Name the blood parasite species.
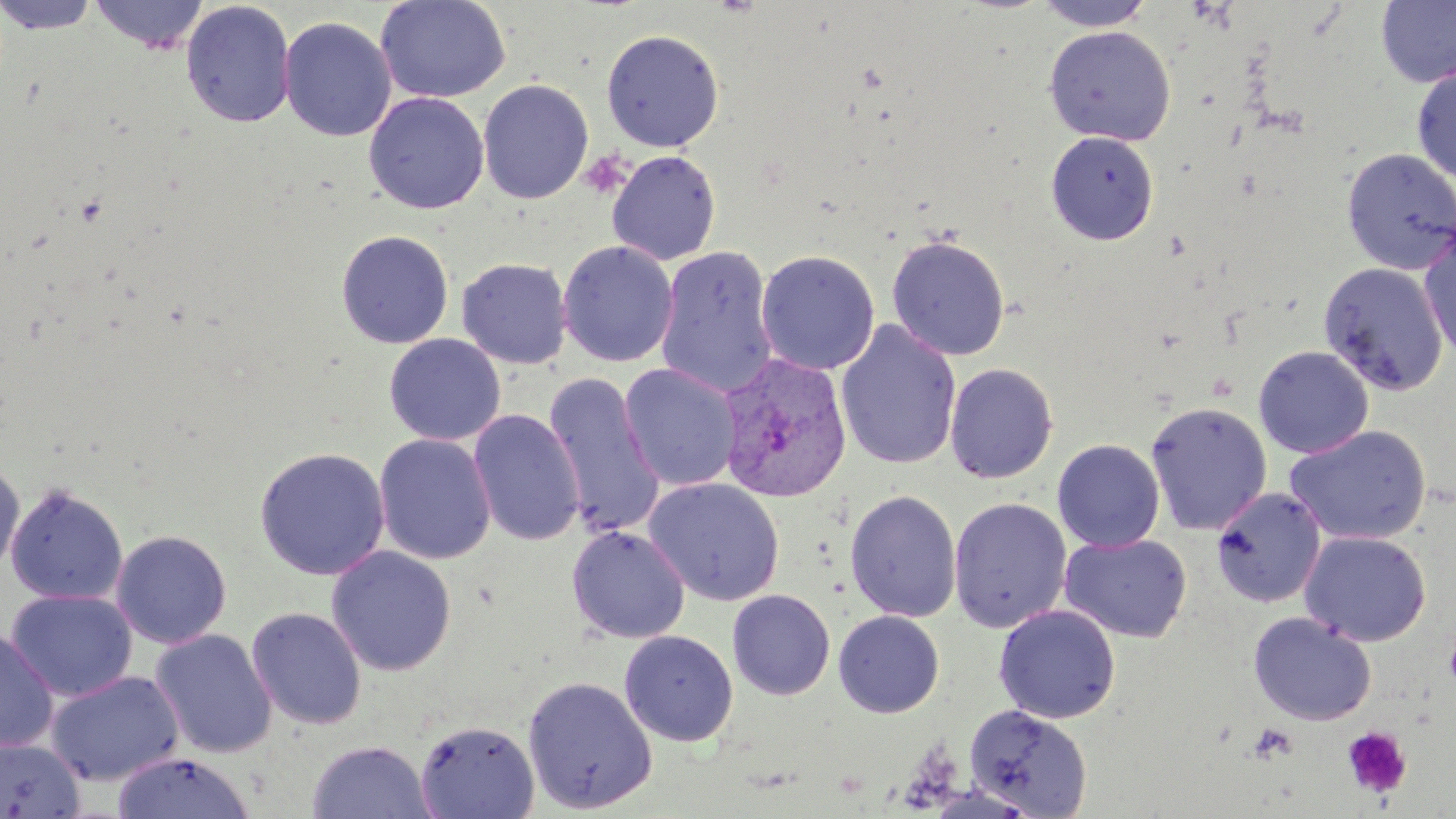
Plasmodium vivax.

uninfected_red_blood_cell_locations: 'approximate bounding boxes as named x1/y1/x2/y2 corners in pixels: (x1=0, y1=0, x2=100, y2=34), (x1=89, y1=0, x2=209, y2=54), (x1=376, y1=0, x2=510, y2=104), (x1=1033, y1=0, x2=1154, y2=31), (x1=1375, y1=0, x2=1456, y2=88), (x1=180, y1=2, x2=296, y2=127), (x1=279, y1=16, x2=397, y2=142), (x1=1043, y1=25, x2=1176, y2=145), (x1=601, y1=29, x2=724, y2=152), (x1=1411, y1=65, x2=1456, y2=185), (x1=478, y1=79, x2=594, y2=204), (x1=364, y1=92, x2=489, y2=214), (x1=1046, y1=131, x2=1159, y2=245), (x1=1341, y1=148, x2=1456, y2=275), (x1=607, y1=150, x2=721, y2=265), (x1=1419, y1=225, x2=1456, y2=365), (x1=335, y1=230, x2=454, y2=349), (x1=886, y1=234, x2=1011, y2=362), (x1=557, y1=241, x2=678, y2=367), (x1=656, y1=245, x2=779, y2=399), (x1=756, y1=250, x2=879, y2=376), (x1=457, y1=258, x2=573, y2=369), (x1=1318, y1=262, x2=1449, y2=396), (x1=835, y1=320, x2=962, y2=470), (x1=383, y1=333, x2=506, y2=445), (x1=1253, y1=345, x2=1374, y2=458), (x1=1264, y1=351, x2=1401, y2=531), (x1=943, y1=362, x2=1058, y2=484), (x1=620, y1=364, x2=740, y2=492), (x1=542, y1=373, x2=665, y2=539), (x1=1145, y1=402, x2=1272, y2=535), (x1=468, y1=409, x2=585, y2=547), (x1=1285, y1=425, x2=1431, y2=545), (x1=374, y1=433, x2=496, y2=565), (x1=1052, y1=439, x2=1165, y2=552), (x1=254, y1=446, x2=391, y2=581), (x1=0, y1=456, x2=24, y2=580), (x1=643, y1=477, x2=785, y2=606), (x1=4, y1=481, x2=128, y2=604), (x1=1211, y1=487, x2=1326, y2=608), (x1=844, y1=490, x2=962, y2=622), (x1=948, y1=497, x2=1072, y2=633), (x1=567, y1=525, x2=691, y2=644), (x1=110, y1=529, x2=232, y2=649), (x1=1299, y1=530, x2=1431, y2=647), (x1=1059, y1=534, x2=1193, y2=642), (x1=326, y1=545, x2=456, y2=676), (x1=4, y1=589, x2=137, y2=702), (x1=727, y1=589, x2=835, y2=700), (x1=994, y1=605, x2=1121, y2=724), (x1=246, y1=607, x2=367, y2=729), (x1=833, y1=610, x2=944, y2=717), (x1=1247, y1=612, x2=1376, y2=726), (x1=0, y1=626, x2=59, y2=754), (x1=150, y1=628, x2=278, y2=759), (x1=619, y1=630, x2=738, y2=747), (x1=46, y1=670, x2=185, y2=786), (x1=522, y1=676, x2=658, y2=813), (x1=964, y1=704, x2=1093, y2=817), (x1=415, y1=719, x2=540, y2=818), (x1=0, y1=737, x2=85, y2=818), (x1=306, y1=740, x2=435, y2=819), (x1=112, y1=751, x2=256, y2=819)'
image_size: 1456×819 pixels
magnification: 1000x
modality: light microscopy
field_of_view: single
plasmodium_vivax_infected_red_blood_cell_locations: 'approximate bounding boxes as named x1/y1/x2/y2 corners in pixels: (x1=716, y1=353, x2=853, y2=502)'
preparation: thin blood smear
stain: May-Grünwald-Giemsa
platelet_locations: 'approximate bounding boxes as named x1/y1/x2/y2 corners in pixels: (x1=578, y1=150, x2=633, y2=200), (x1=1247, y1=723, x2=1299, y2=764), (x1=1342, y1=726, x2=1412, y2=799)'